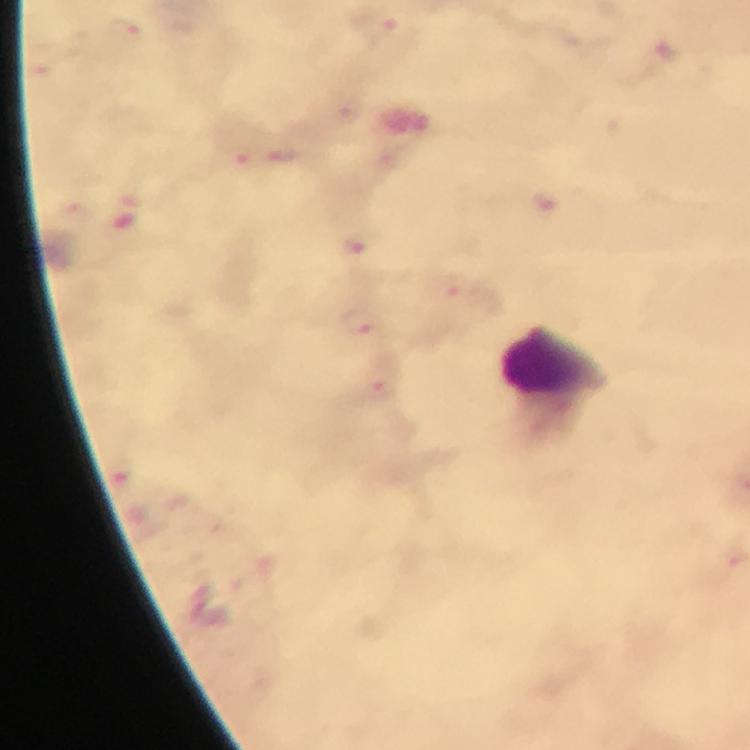

Approximate centers as [x, y] in pixels.
Summary:
  - Leukocyte locations: [555, 363]
  - Plasmodium parasite locations: [380, 24], [128, 31], [666, 54], [282, 158], [546, 204], [446, 286], [364, 321], [380, 381]
  - Image size: 750×750 pixels
  - Preparation: thick smear
  - Capture: smartphone camera through the microscope
  - Magnification: 100x
  - Immersion oil: used
  - Cropped from: a single field of view
  - Context: from a malaria diagnostic workup
  - Stain: Giemsa